Point out every malaria parasite.
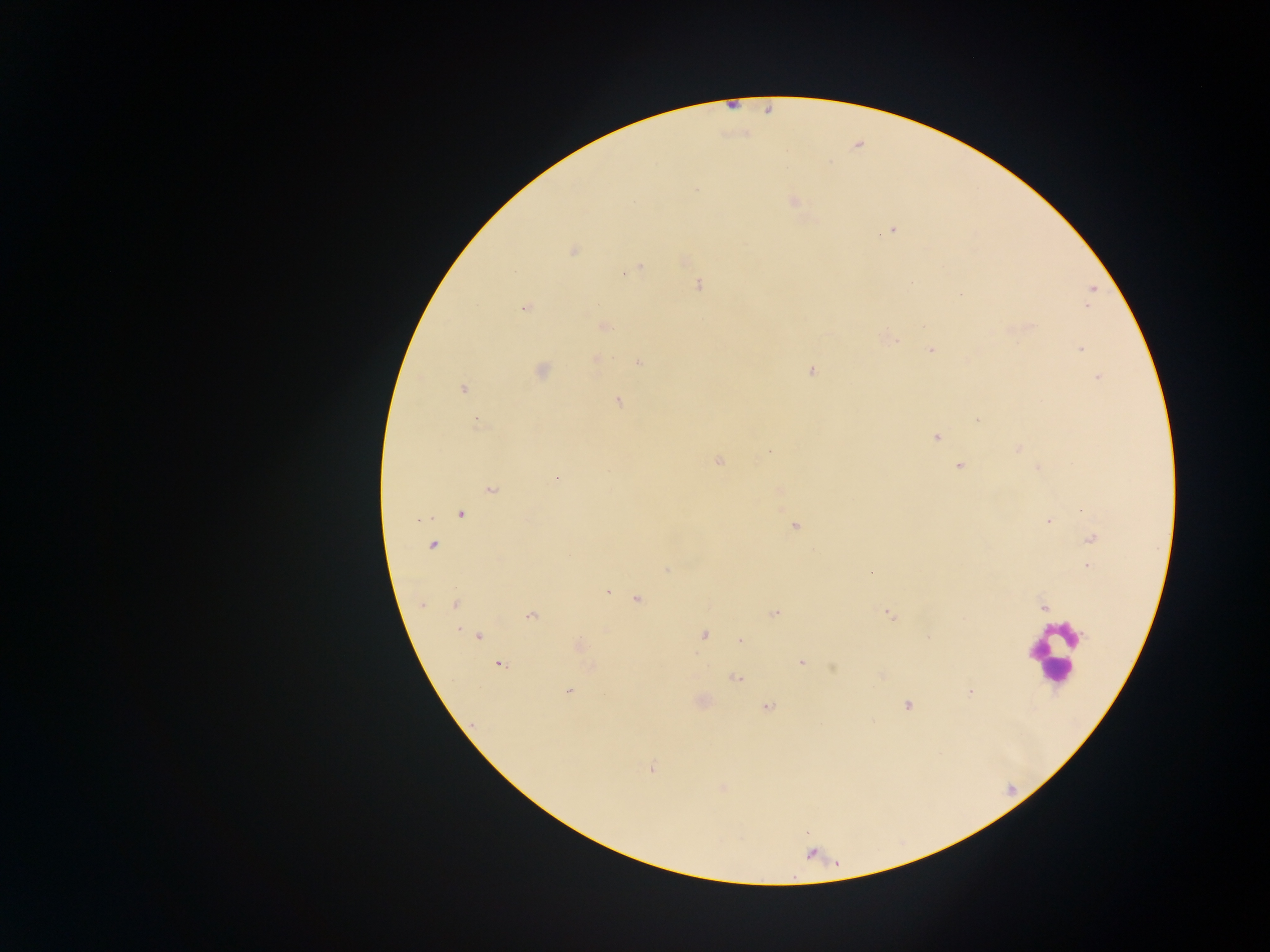

Approximate centers as [x, y] in pixels.
Malaria parasites: [696, 189], [793, 201], [891, 231], [883, 232], [573, 251], [639, 267], [630, 271], [624, 274], [911, 283], [699, 285], [1092, 289], [960, 294], [1086, 307], [524, 308], [603, 326], [889, 338], [931, 350], [1081, 350], [596, 359], [639, 363], [542, 371], [811, 371], [1099, 378], [463, 389], [617, 401], [978, 420], [477, 424], [936, 438], [1019, 448], [770, 451], [718, 461], [959, 465], [1038, 467], [556, 479], [491, 490], [460, 514], [419, 520], [1047, 521], [794, 527], [1091, 538], [432, 545], [1088, 566], [666, 570], [608, 593], [638, 599], [422, 604], [455, 604], [1043, 607], [776, 612], [888, 613], [531, 616], [459, 630], [704, 635], [478, 636], [740, 641], [579, 646], [801, 663], [500, 665], [833, 668], [736, 678], [569, 691], [970, 691], [907, 705], [767, 707], [651, 768], [723, 788].

Leukocyte locations: [1054, 654]. Photographed through a microscope with a mobile-phone camera. Single field of view. Image is 1270×952 pixels. Sample from Ghana. Thick blood smear.